Classify this cell by malaria status.
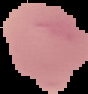
Uninfected.

image type = cell region segmented out of the field of view; surrounding area masked to black
preparation = thin blood smear
image size = 88×94 pixels